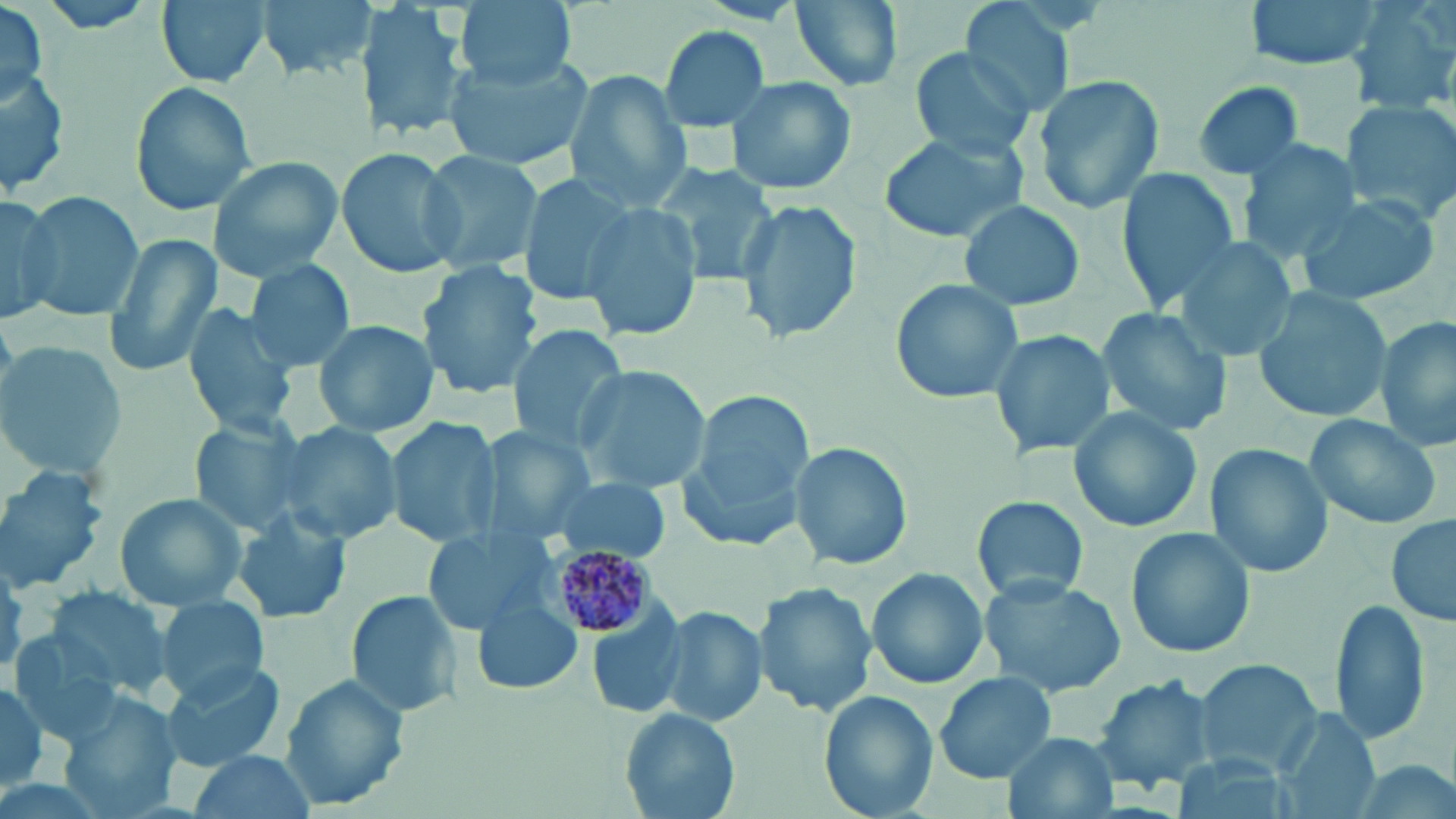

Approximate bounding boxes as (x1, y1, x2, y2) in pixels. Plasmodium malariae-infected red blood cell locations: (545, 547, 661, 640). Uninfected red blood cell locations: (29, 0, 163, 36), (155, 0, 270, 89), (258, 0, 375, 82), (356, 0, 472, 145), (454, 0, 577, 88), (789, 0, 903, 92), (1246, 0, 1383, 72), (1352, 0, 1456, 112), (959, 1, 1077, 117), (2, 6, 49, 110), (659, 26, 770, 132), (911, 46, 1040, 157), (441, 51, 593, 168), (0, 69, 70, 196), (565, 71, 692, 214), (726, 75, 855, 196), (1030, 75, 1166, 216), (1188, 79, 1308, 181), (129, 82, 257, 218), (1341, 99, 1455, 216), (875, 130, 1027, 244), (1238, 139, 1361, 263), (336, 145, 466, 281), (421, 149, 547, 276), (209, 156, 342, 282), (653, 163, 777, 284), (1116, 168, 1242, 312), (515, 174, 632, 303), (19, 191, 145, 324), (1296, 192, 1441, 307), (0, 193, 60, 323), (736, 198, 861, 346), (957, 199, 1084, 311), (582, 201, 702, 343), (1174, 234, 1304, 363), (104, 235, 223, 381), (247, 258, 355, 372), (418, 261, 544, 400), (889, 277, 1024, 405), (1252, 289, 1393, 424), (181, 304, 298, 436), (1097, 307, 1231, 437), (1376, 315, 1455, 452), (312, 318, 439, 438), (505, 325, 628, 453), (988, 327, 1113, 461), (0, 343, 126, 479), (574, 365, 710, 493), (682, 393, 814, 549), (1066, 407, 1205, 535), (1305, 412, 1446, 530), (186, 415, 309, 536), (387, 416, 503, 548), (280, 422, 404, 546), (477, 424, 592, 538), (789, 442, 913, 573), (1205, 445, 1333, 578), (0, 466, 109, 593), (547, 478, 673, 563), (112, 491, 248, 609), (972, 495, 1089, 605), (232, 506, 352, 625), (1386, 514, 1455, 629), (422, 527, 545, 635), (1125, 527, 1256, 660), (866, 568, 991, 689), (980, 577, 1127, 697), (754, 582, 877, 719), (41, 584, 175, 697), (346, 591, 465, 720), (154, 594, 270, 702), (471, 597, 584, 697), (1329, 598, 1432, 747), (660, 608, 767, 728), (586, 617, 689, 720), (6, 629, 125, 747), (1193, 659, 1321, 777), (158, 662, 291, 769), (933, 672, 1058, 783), (1092, 673, 1222, 794), (282, 675, 409, 811), (0, 682, 52, 792), (63, 689, 178, 814), (819, 691, 938, 818), (620, 708, 738, 818), (1269, 709, 1382, 819), (1005, 732, 1117, 819), (179, 751, 313, 819), (1168, 755, 1300, 819). Slide-level diagnosis: Plasmodium malariae. May-Grünwald-Giemsa stain. Image is 1456×819 pixels. Light microscopy. Thin blood film. Single field of view. Captured at 1000x magnification.